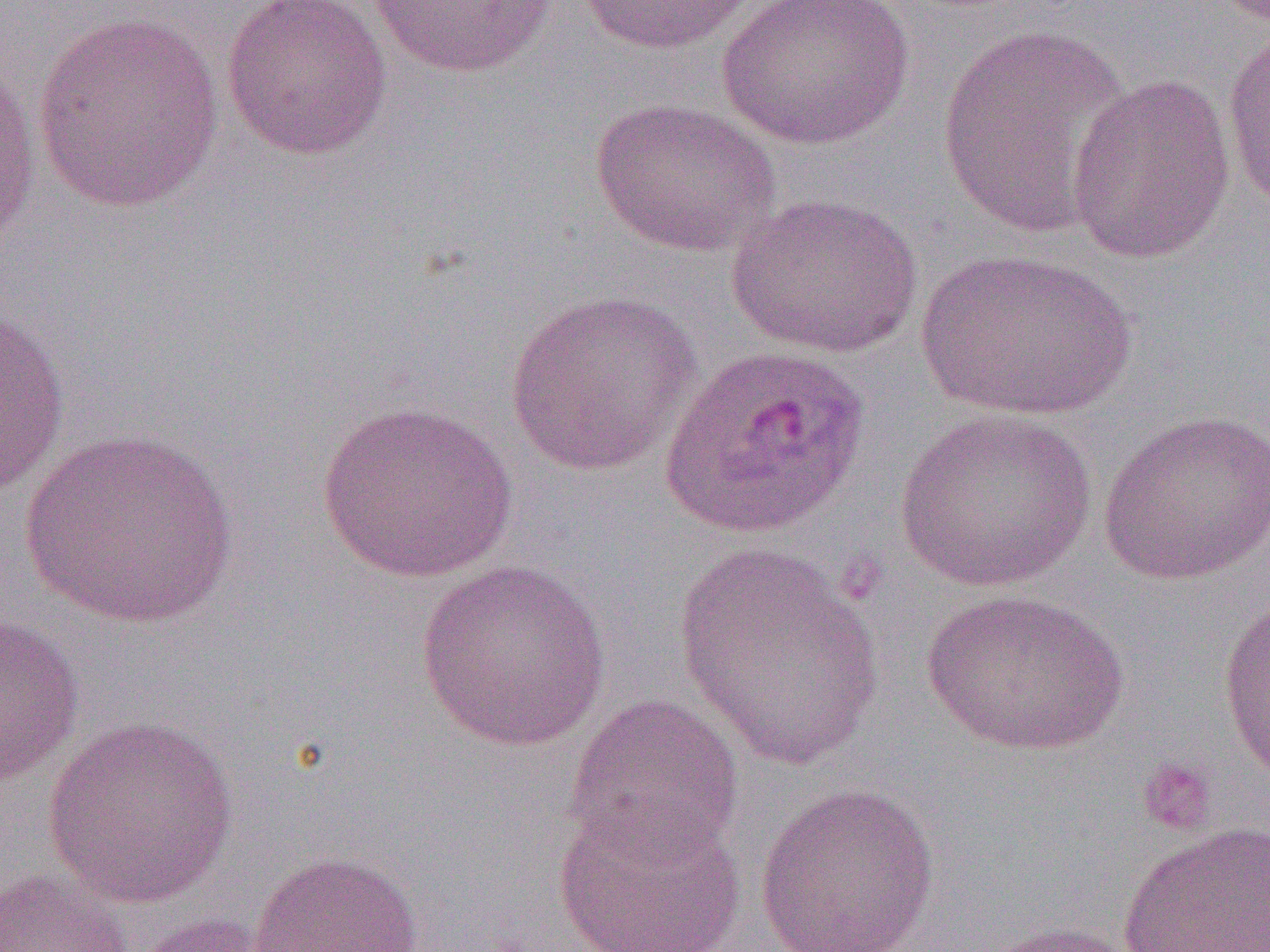

Approximate bounding boxes as (x1, y1, x2, y2) in pixels. Uninfected red blood cell locations: (219, 0, 394, 162), (572, 0, 762, 55), (714, 0, 918, 150), (366, 1, 560, 78), (32, 9, 226, 212), (935, 21, 1134, 240), (1221, 25, 1270, 214), (0, 51, 42, 256), (1066, 72, 1236, 264), (589, 97, 782, 258), (726, 190, 927, 359), (917, 248, 1138, 422), (503, 289, 703, 478), (0, 303, 70, 500), (316, 400, 521, 583), (894, 407, 1096, 592), (1097, 409, 1270, 586), (19, 429, 241, 631), (675, 545, 887, 770), (415, 560, 611, 751), (920, 588, 1130, 756), (1218, 589, 1270, 786), (0, 612, 84, 787), (565, 690, 744, 863), (42, 716, 238, 909), (752, 781, 941, 952), (553, 794, 747, 952), (1118, 821, 1269, 952), (247, 850, 425, 951), (0, 868, 134, 952), (130, 912, 285, 952), (973, 920, 1145, 952). Platelet locations: (1136, 758, 1219, 836). Plasmodium ovale-infected red blood cell locations: (660, 343, 873, 539). Slide-level diagnosis: Plasmodium ovale. Single field of view. 1000x magnification. Image is 1270×952 pixels. Optical microscopy. Thin blood film.